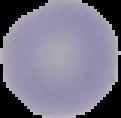
{
  "preparation": "thin blood film",
  "result": "no malaria parasites seen",
  "image_type": "cell region segmented out of the field of view; surrounding area masked to black",
  "image_size": "121×118 pixels"
}